Assess the morphology of the erythrocytes.
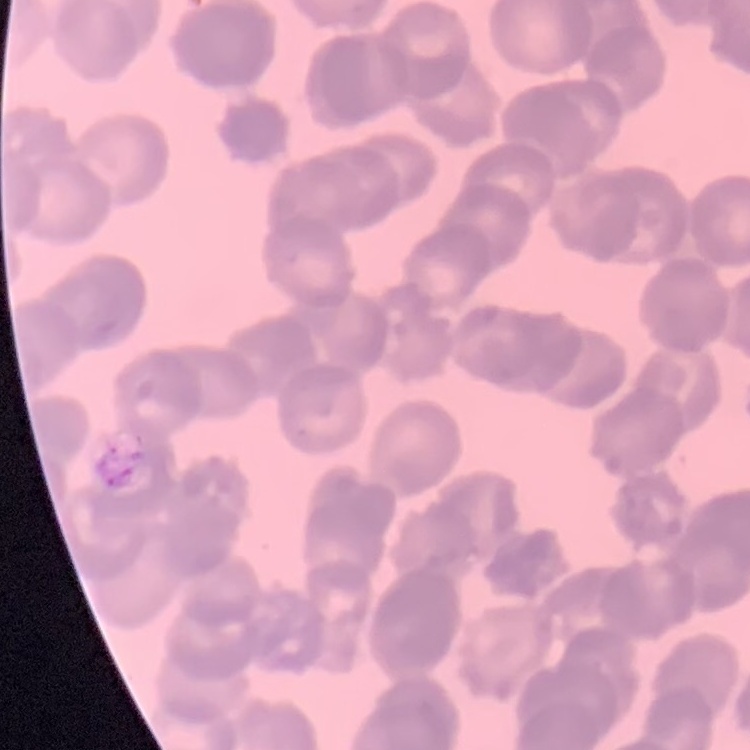

They show rouleaux formation.

preparation = thin blood film
image type = square crop of a larger photomicrograph
stain = Field's or Giemsa